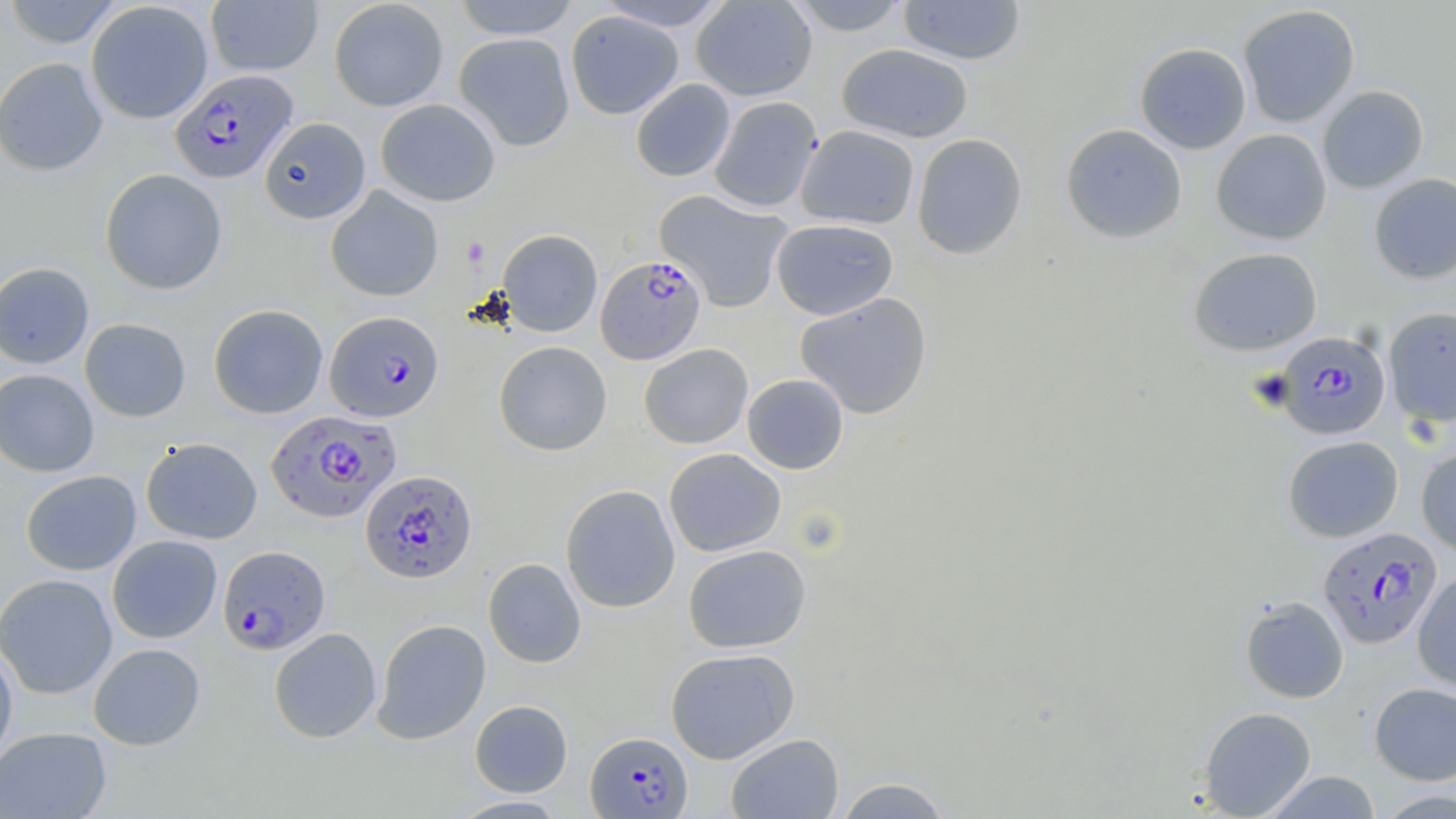
Summary:
  - Coordinate format: approximate bounding boxes as (x1, y1, x2, y2) in pixels
  - Uninfected red blood cell locations: (1, 0, 126, 49), (328, 0, 448, 111), (451, 0, 581, 39), (595, 0, 734, 31), (691, 0, 818, 101), (785, 0, 911, 36), (898, 0, 1026, 65), (205, 1, 323, 76), (86, 2, 213, 124), (1237, 4, 1361, 128), (565, 10, 684, 119), (454, 32, 575, 151), (1134, 42, 1252, 154), (836, 43, 974, 143), (0, 57, 108, 176), (630, 79, 736, 182), (1317, 85, 1429, 193), (709, 96, 822, 213), (375, 98, 500, 206), (259, 117, 371, 223), (1061, 123, 1187, 243), (796, 125, 920, 229), (1211, 128, 1332, 245), (912, 133, 1028, 260), (100, 169, 227, 294), (1369, 173, 1456, 284), (326, 186, 444, 302), (655, 189, 793, 313), (771, 218, 898, 320), (497, 229, 603, 336), (1188, 247, 1322, 355), (0, 261, 94, 369), (795, 293, 932, 419), (208, 304, 328, 419), (1383, 306, 1456, 427), (79, 318, 191, 422), (494, 341, 612, 456), (639, 343, 753, 449), (0, 369, 99, 477), (742, 374, 849, 474), (1282, 435, 1404, 542), (141, 437, 263, 544), (1416, 446, 1456, 556), (664, 448, 786, 557), (20, 470, 141, 575), (560, 484, 681, 613), (107, 535, 222, 643), (683, 544, 811, 653), (483, 558, 586, 668), (1413, 571, 1455, 693), (0, 573, 117, 699), (1240, 596, 1349, 703), (372, 619, 491, 744), (269, 627, 382, 743), (88, 642, 206, 750), (0, 644, 18, 771), (665, 648, 799, 764), (1370, 682, 1456, 785), (470, 699, 573, 797), (1199, 706, 1317, 818), (0, 726, 112, 818), (726, 733, 844, 819), (1260, 770, 1382, 818), (833, 776, 953, 818), (1374, 788, 1456, 817), (449, 795, 570, 818)
  - Platelet locations: (462, 237, 490, 266)
  - Plasmodium falciparum-infected red blood cell locations: (171, 70, 297, 183), (595, 255, 706, 365), (325, 310, 444, 422), (1274, 330, 1391, 439), (267, 409, 400, 523), (360, 469, 477, 583), (1317, 525, 1443, 648), (218, 545, 331, 655), (586, 731, 693, 818)
  - Slide-level diagnosis: Plasmodium falciparum
  - Preparation: thin blood smear
  - Image size: 1456×819 pixels
  - Modality: optical microscopy
  - Field of view: single
  - Magnification: 1000x
  - Stain: May-Grünwald-Giemsa